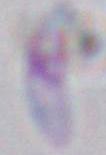
{
  "identification": "Toxoplasma gondii",
  "modality": "micrograph",
  "magnification": "1000x"
}